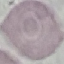 Result: no malaria parasites seen. Automatically extracted cell patch, resized to 64 × 64 pixels. Thin smear of blood. Acquired by smartphone through the microscope eyepiece. Giemsa-stained preparation.